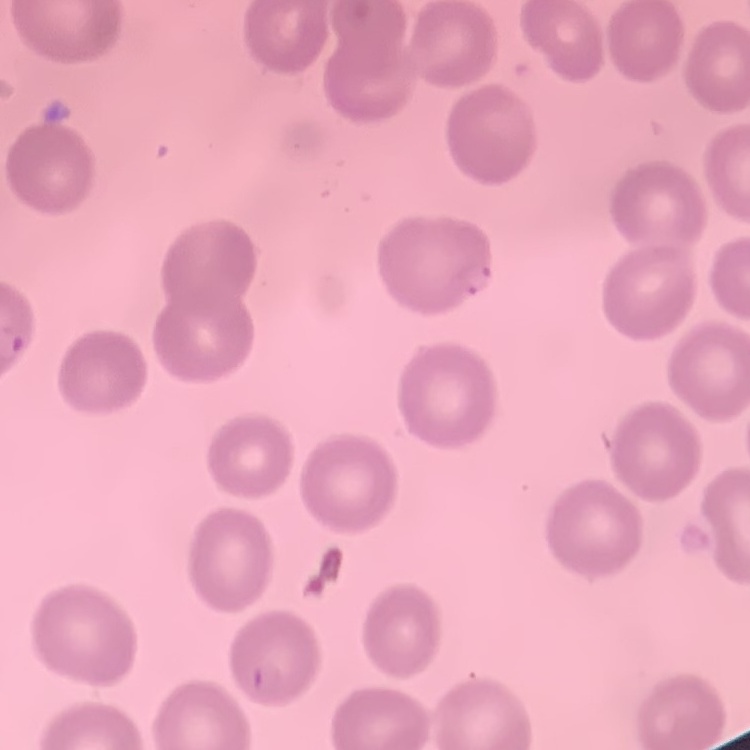

{
  "erythrocyte_morphology": "no rouleaux formation",
  "preparation": "thin peripheral smear",
  "image_type": "square crop of a larger photomicrograph",
  "stain": "Field's or Giemsa"
}